Comment on the background quality.
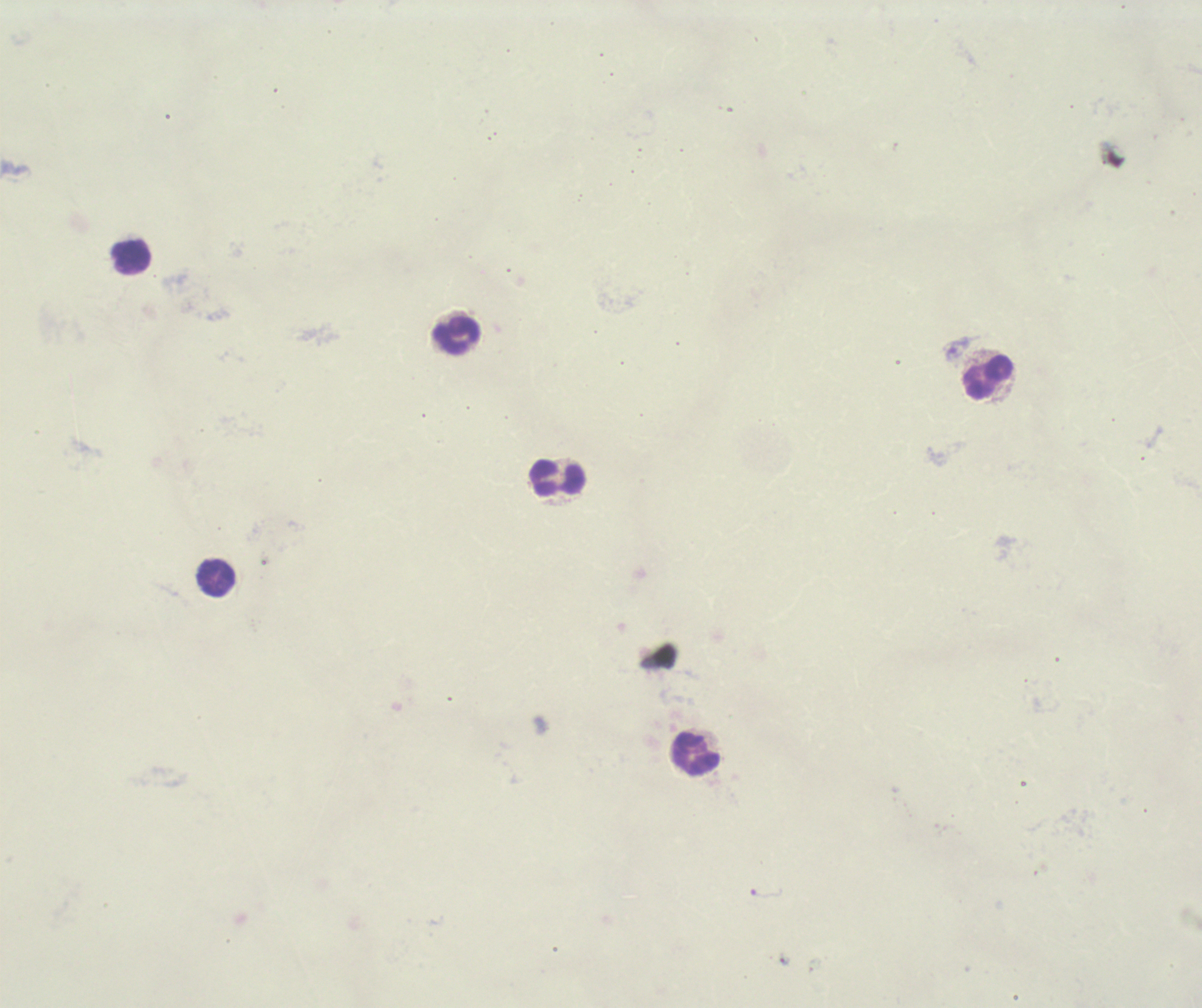

Poor.

Approximate centers as {x, y} in pixels. Leukocyte locations: {131, 257}, {458, 336}, {988, 378}, {558, 479}, {217, 577}, {697, 754}. Single field of view. Thick smear of blood. Previously used in a real diagnosis. Romanowsky stain. Result: no malaria parasites seen. 100x magnification. Image is 1202×1008 pixels.